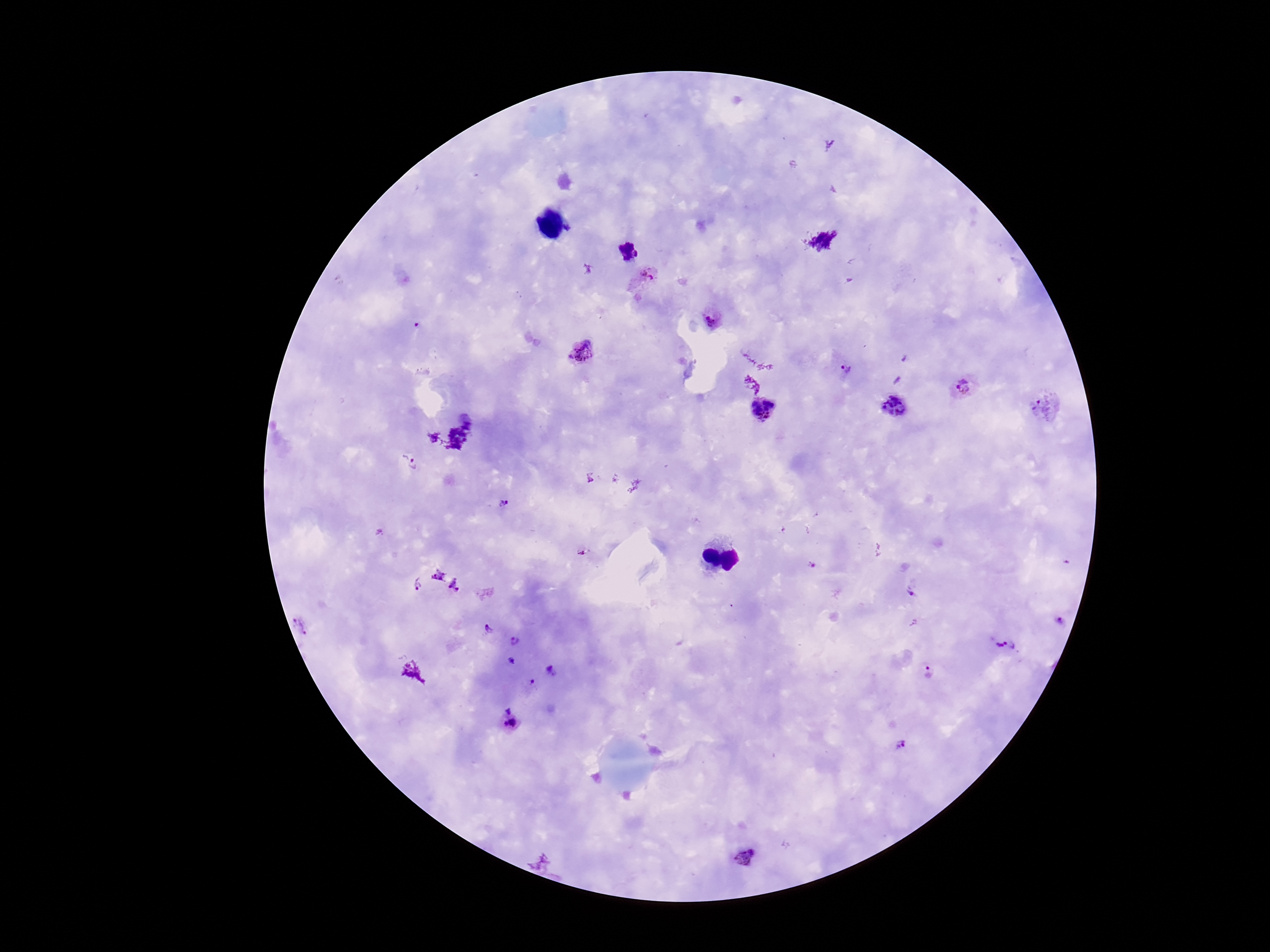
{
  "magnification": "100x",
  "image_size": "1270×952 pixels",
  "capture": "smartphone camera through the microscope eyepiece",
  "preparation": "thick peripheral-blood smear",
  "stain": "Giemsa",
  "patient_malaria_status": "infected",
  "field_of_view": "one from this slide",
  "plasmodium_parasite_locations": "approximate object centers, in pixels from the top-left corner: (x=626, y=251), (x=643, y=277), (x=711, y=320), (x=419, y=326), (x=585, y=353), (x=845, y=370), (x=964, y=386), (x=1044, y=406), (x=894, y=408), (x=764, y=409), (x=415, y=464), (x=502, y=504), (x=583, y=552), (x=446, y=580), (x=416, y=585), (x=914, y=591), (x=1059, y=621), (x=488, y=629), (x=516, y=641), (x=1001, y=644), (x=512, y=660), (x=550, y=671), (x=929, y=672), (x=533, y=682), (x=507, y=707), (x=511, y=724), (x=902, y=745), (x=747, y=859)"
}